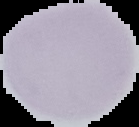
Summary:
  - Image size: 139×127 pixels
  - Malaria status: uninfected
  - Image type: segmented cell region with the area outside set to black
  - Preparation: thin blood film